Assess this cell for malaria.
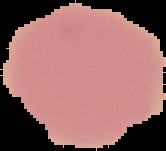

Uninfected.

Summary:
  - Image size: 166×151 pixels
  - Image type: segmented cell region with the area outside set to black
  - Preparation: thin blood film